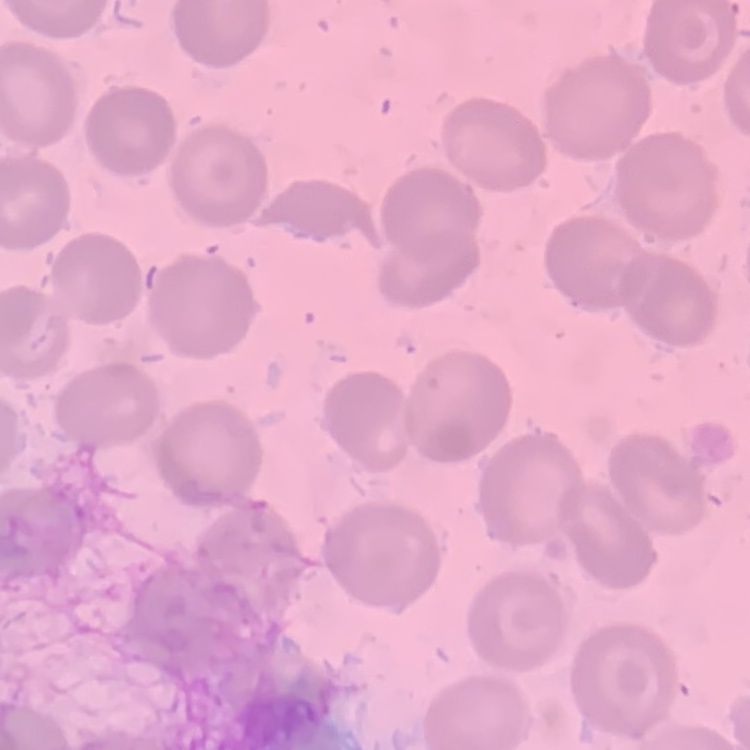

The red blood cells exhibit no rouleaux formation. Field's or Giemsa stain. Square crop of a larger photomicrograph. Thin peripheral smear.